Identify the blood parasite species.
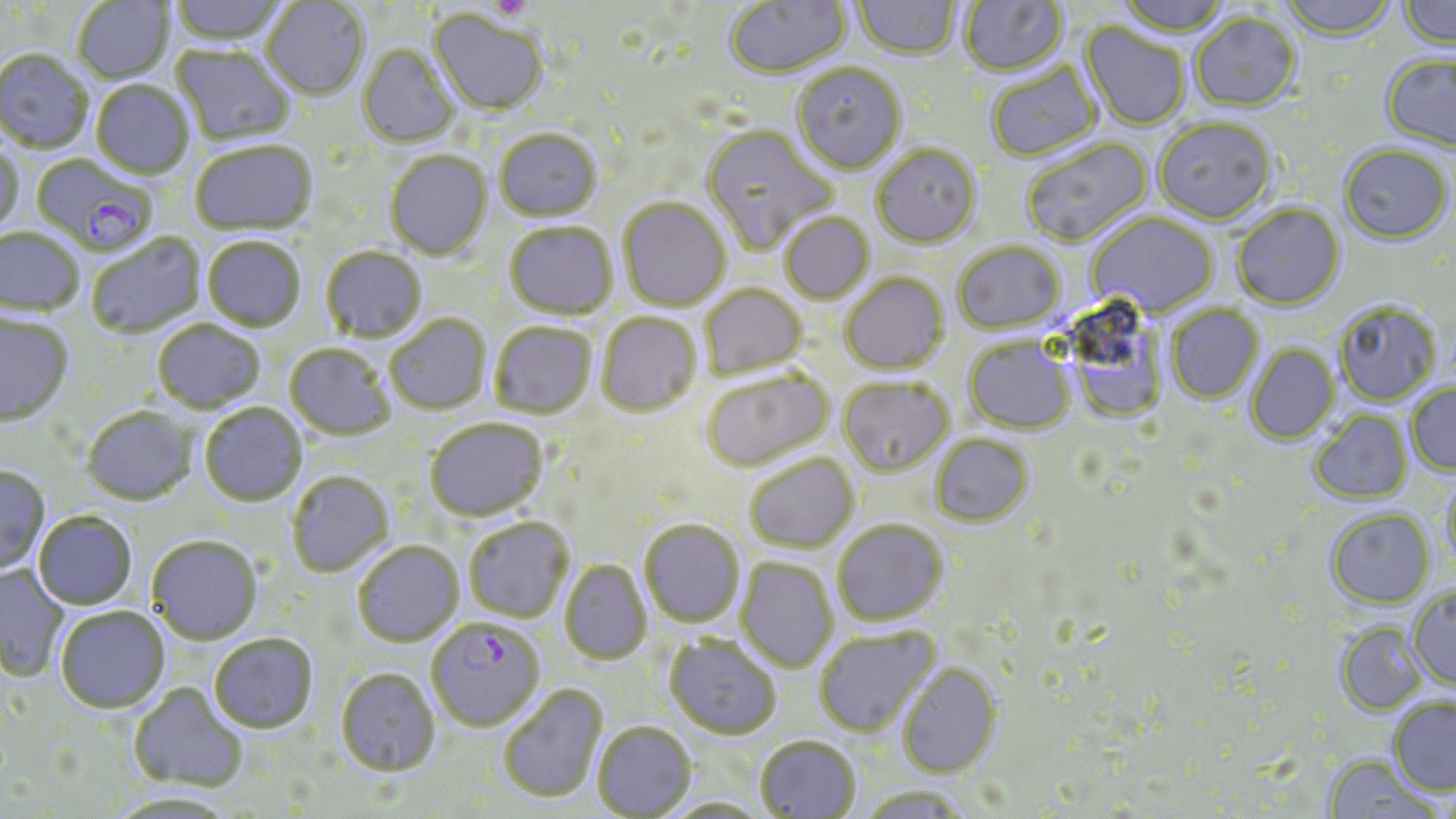
Plasmodium falciparum.

Approximate bounding boxes as [x1, y1, x2, y2] in pixels. Uninfected red blood cell locations: [72, 0, 173, 83], [168, 0, 288, 46], [724, 0, 851, 80], [959, 0, 1070, 79], [1115, 0, 1232, 38], [1278, 0, 1396, 43], [1399, 0, 1456, 52], [262, 1, 369, 100], [853, 1, 960, 61], [429, 11, 547, 117], [1189, 14, 1301, 113], [1079, 22, 1190, 131], [357, 45, 459, 148], [171, 46, 295, 147], [0, 49, 94, 154], [1380, 54, 1456, 154], [986, 62, 1102, 163], [792, 64, 906, 176], [91, 81, 193, 179], [1154, 120, 1276, 225], [702, 126, 836, 256], [494, 130, 602, 222], [1021, 138, 1154, 248], [0, 141, 26, 238], [190, 141, 317, 236], [871, 145, 981, 250], [1338, 146, 1453, 247], [385, 150, 492, 260], [618, 198, 731, 312], [1232, 204, 1345, 311], [779, 213, 875, 305], [1086, 213, 1219, 317], [505, 221, 617, 319], [0, 227, 85, 317], [86, 233, 206, 338], [203, 236, 306, 332], [953, 243, 1066, 336], [321, 246, 427, 343], [841, 272, 948, 376], [700, 283, 807, 379], [1334, 304, 1441, 406], [1166, 305, 1264, 403], [596, 312, 701, 416], [0, 313, 74, 426], [385, 314, 491, 414], [1082, 314, 1168, 426], [153, 320, 265, 412], [489, 322, 596, 418], [964, 336, 1074, 434], [285, 343, 395, 440], [1246, 343, 1340, 444], [700, 369, 835, 473], [838, 378, 953, 477], [1405, 383, 1456, 476], [200, 403, 307, 506], [82, 405, 196, 505], [1310, 410, 1412, 504], [425, 418, 548, 521], [931, 433, 1033, 526], [745, 454, 859, 553], [0, 466, 51, 575], [287, 471, 394, 577], [1441, 475, 1456, 576], [1326, 510, 1435, 608], [34, 512, 137, 610], [463, 517, 574, 623], [639, 519, 744, 627], [832, 519, 948, 625], [147, 535, 262, 644], [352, 540, 464, 647], [736, 557, 837, 672], [560, 560, 652, 663], [0, 565, 69, 682], [1407, 586, 1456, 691], [55, 607, 170, 714], [1335, 622, 1428, 715], [813, 626, 941, 737], [208, 634, 318, 734], [664, 634, 781, 740], [897, 661, 1002, 778], [336, 667, 440, 776], [498, 682, 608, 804], [128, 683, 248, 793], [1387, 698, 1456, 797], [592, 721, 696, 818], [754, 735, 860, 818], [1322, 756, 1439, 819], [857, 785, 972, 819], [105, 792, 238, 818], [661, 797, 770, 818]. Platelet locations: [488, 0, 531, 21]. Plasmodium falciparum-infected red blood cell locations: [31, 154, 158, 256], [426, 617, 544, 731]. 1000x magnification. Thin blood smear. Image is 1456×819 pixels. May-Grünwald-Giemsa stain. Single field of view. Light microscopy.